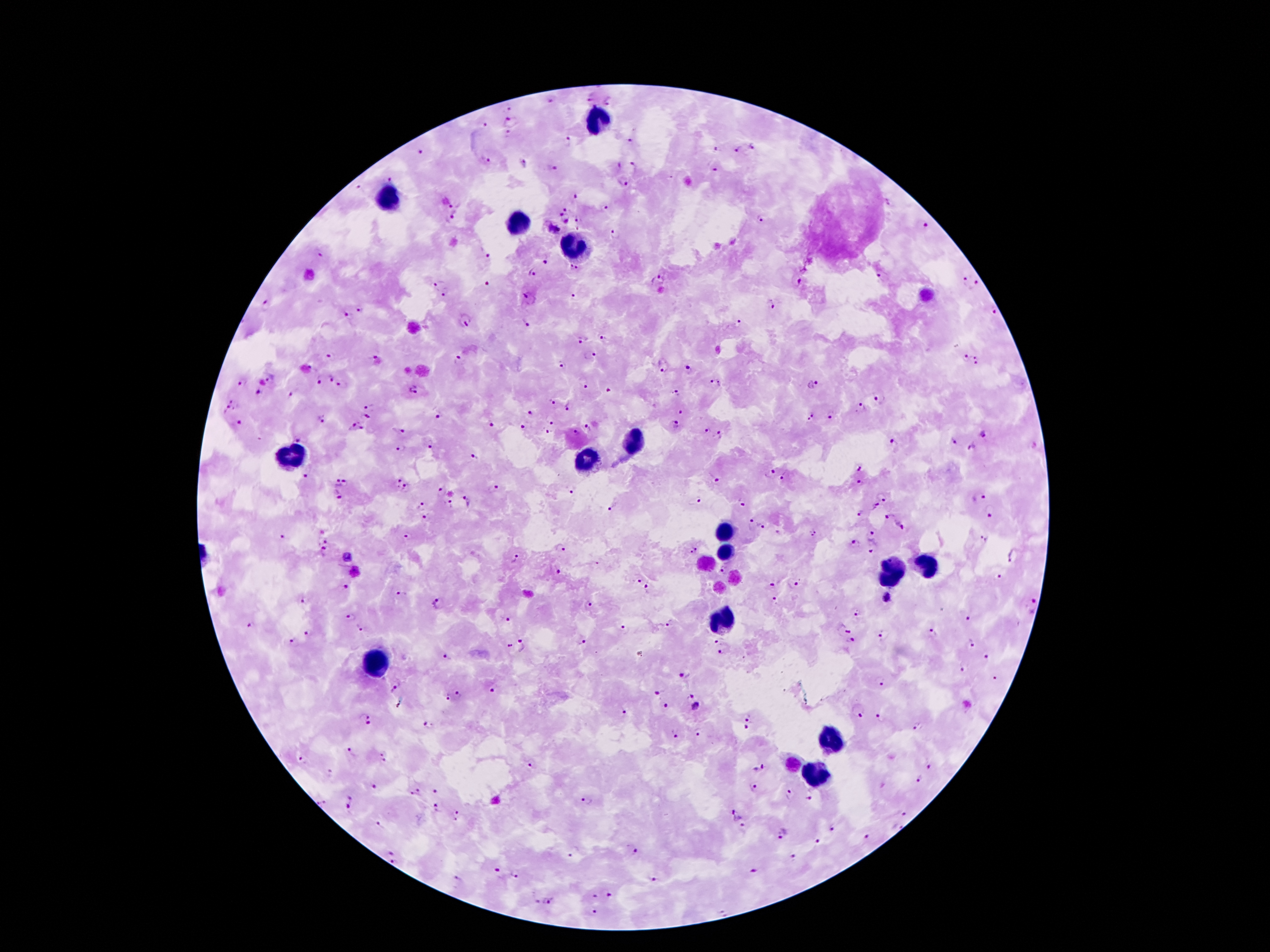
malaria_parasite_locations: 'approximate centers as {x, y} in pixels: {590, 99}, {550, 102}, {610, 102}, {509, 107}, {510, 121}, {484, 126}, {508, 135}, {631, 141}, {568, 142}, {754, 147}, {715, 150}, {739, 150}, {420, 153}, {486, 160}, {523, 163}, {616, 165}, {635, 165}, {553, 167}, {715, 169}, {391, 179}, {624, 182}, {358, 187}, {576, 196}, {455, 201}, {605, 207}, {567, 208}, {456, 215}, {560, 215}, {580, 218}, {567, 220}, {762, 220}, {926, 228}, {553, 229}, {578, 229}, {614, 233}, {321, 253}, {490, 256}, {545, 258}, {574, 268}, {532, 272}, {880, 276}, {661, 281}, {796, 281}, {487, 282}, {438, 283}, {965, 283}, {977, 287}, {444, 294}, {525, 296}, {574, 297}, {772, 304}, {267, 306}, {359, 311}, {995, 314}, {347, 315}, {465, 323}, {526, 323}, {737, 323}, {602, 337}, {582, 338}, {330, 354}, {590, 355}, {374, 356}, {967, 357}, {459, 360}, {978, 360}, {561, 365}, {665, 369}, {689, 370}, {271, 377}, {328, 378}, {242, 379}, {317, 379}, {714, 382}, {815, 383}, {343, 385}, {583, 385}, {415, 390}, {609, 390}, {677, 392}, {258, 393}, {292, 394}, {236, 400}, {551, 400}, {879, 400}, {370, 404}, {862, 405}, {569, 406}, {225, 409}, {531, 413}, {681, 413}, {440, 416}, {830, 416}, {365, 417}, {812, 418}, {322, 419}, {552, 422}, {239, 424}, {491, 425}, {676, 425}, {521, 427}, {588, 427}, {355, 428}, {401, 431}, {547, 432}, {576, 433}, {705, 433}, {719, 435}, {983, 436}, {300, 437}, {953, 439}, {894, 443}, {431, 445}, {971, 448}, {400, 452}, {475, 455}, {859, 471}, {771, 473}, {785, 477}, {305, 478}, {714, 479}, {396, 481}, {336, 483}, {345, 485}, {861, 485}, {408, 487}, {493, 487}, {441, 490}, {574, 492}, {339, 496}, {884, 498}, {979, 498}, {695, 501}, {467, 502}, {742, 503}, {448, 504}, {424, 506}, {875, 506}, {611, 507}, {861, 512}, {988, 514}, {889, 517}, {751, 522}, {762, 527}, {902, 527}, {812, 533}, {874, 534}, {407, 537}, {278, 538}, {982, 538}, {326, 540}, {854, 545}, {561, 547}, {874, 549}, {694, 551}, {324, 552}, {1013, 556}, {515, 558}, {723, 571}, {559, 573}, {999, 577}, {638, 580}, {794, 584}, {772, 585}, {345, 586}, {650, 588}, {401, 592}, {888, 597}, {303, 600}, {774, 600}, {439, 604}, {1030, 605}, {589, 606}, {350, 616}, {858, 616}, {967, 618}, {506, 619}, {252, 624}, {669, 624}, {361, 627}, {844, 628}, {625, 629}, {932, 633}, {308, 634}, {881, 636}, {290, 641}, {716, 641}, {582, 642}, {852, 642}, {971, 642}, {509, 644}, {523, 646}, {720, 652}, {446, 656}, {984, 656}, {962, 670}, {685, 673}, {995, 677}, {880, 682}, {395, 687}, {492, 691}, {655, 692}, {459, 693}, {447, 696}, {691, 697}, {665, 706}, {696, 707}, {858, 709}, {622, 713}, {747, 715}, {364, 718}, {882, 718}, {428, 723}, {746, 727}, {918, 727}, {698, 733}, {673, 735}, {352, 751}, {384, 756}, {303, 759}, {530, 764}, {759, 768}, {929, 768}, {919, 779}, {374, 787}, {753, 789}, {436, 791}, {786, 793}, {414, 794}, {809, 799}, {587, 801}, {350, 802}, {324, 803}, {438, 807}, {459, 814}, {903, 814}, {735, 815}, {377, 825}, {897, 826}, {830, 827}, {743, 828}, {782, 834}, {867, 838}, {815, 842}, {634, 852}, {391, 854}, {571, 855}, {795, 858}, {392, 861}, {496, 870}, {754, 871}, {514, 875}, {457, 879}, {652, 880}, {608, 894}, {594, 898}, {549, 902}, {594, 911}, {722, 912}'
leukocyte_locations: 'approximate centers as {x, y} in pixels: {595, 119}, {388, 201}, {519, 221}, {579, 245}, {633, 441}, {287, 453}, {589, 458}, {722, 533}, {724, 552}, {930, 568}, {892, 570}, {722, 617}, {379, 664}, {832, 738}, {818, 772}'
preparation: thick blood smear
stain: Giemsa
magnification: 100x
capture: smartphone through the microscope eyepiece
image_size: 1270×952 pixels
field_of_view: single
patient_malaria_status: infected with Plasmodium falciparum